Locate and identify every blood parasite.
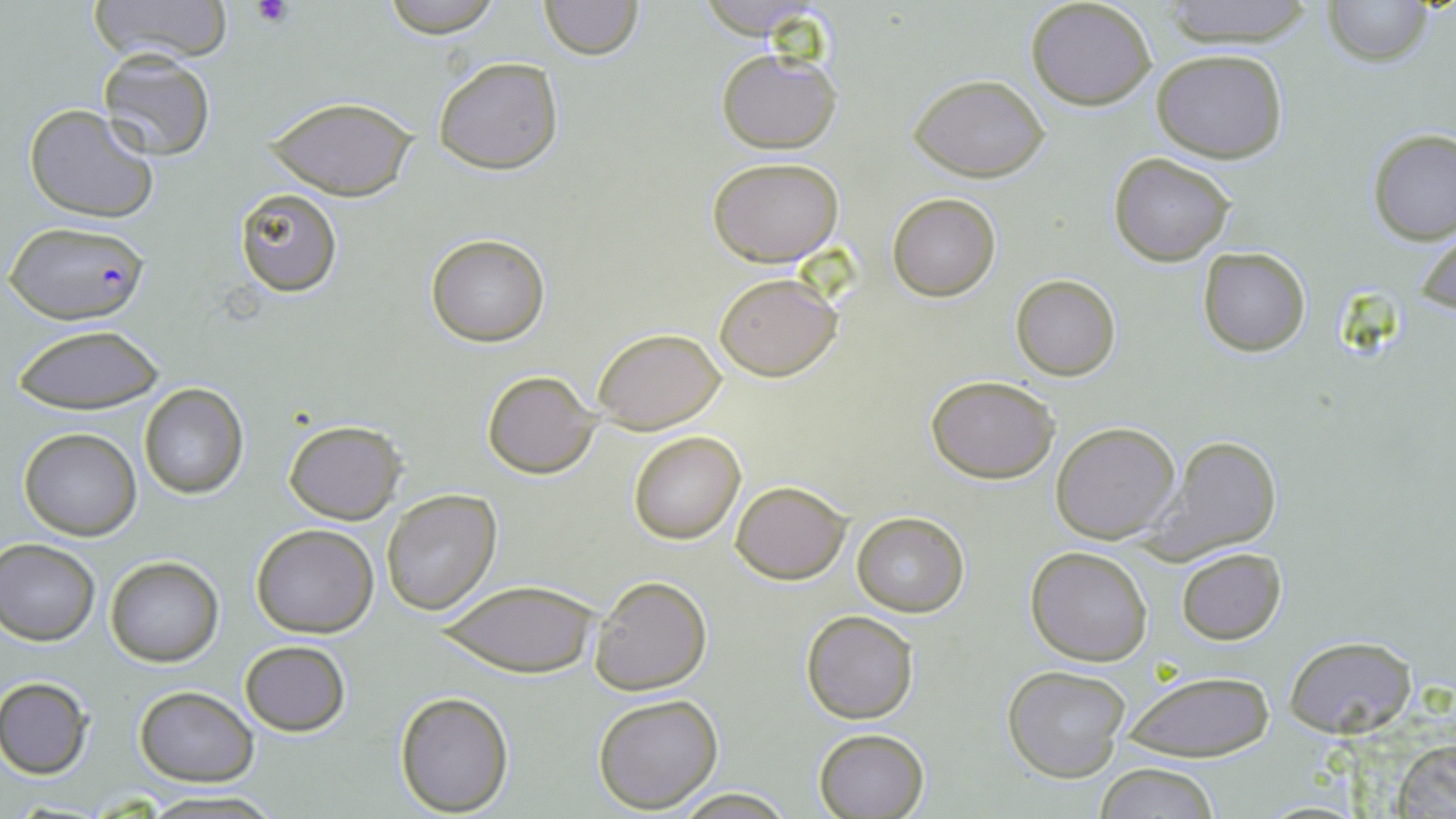

Approximate bounding boxes as (x1,y1)-(x2,y2) corner pairs in pixels.
Plasmodium falciparum-infected red blood cells: (3,220)-(150,325).
No Plasmodium ovale, Plasmodium malariae, Plasmodium vivax, Babesia divergens, or Trypanosoma brucei observed.

Uninfected red blood cell locations: (94,0)-(229,65), (376,0)-(508,39), (691,0)-(834,40), (1158,0)-(1318,47), (1323,0)-(1434,67), (537,1)-(644,60), (1025,1)-(1158,111), (716,48)-(842,154), (1153,49)-(1288,163), (96,50)-(216,161), (432,57)-(563,173), (909,73)-(1051,183), (267,96)-(416,201), (24,103)-(159,223), (1366,128)-(1455,243), (1108,153)-(1236,265), (707,157)-(845,266), (234,188)-(342,296), (887,193)-(1000,300), (1415,224)-(1456,322), (426,234)-(548,346), (1198,247)-(1310,355), (714,273)-(841,380), (1011,275)-(1121,381), (12,324)-(166,414), (593,326)-(727,434), (481,370)-(601,478), (924,373)-(1060,482), (138,385)-(248,498), (283,419)-(406,525), (1050,421)-(1181,544), (20,428)-(142,539), (628,429)-(747,545), (1149,436)-(1282,557), (730,480)-(849,584), (380,489)-(502,615), (852,511)-(969,617), (250,524)-(379,638), (0,539)-(100,644), (1024,546)-(1153,666), (1175,548)-(1286,644), (105,556)-(223,667), (587,573)-(712,697), (437,579)-(599,677), (801,610)-(919,722), (1284,635)-(1417,737), (239,640)-(351,737), (1003,665)-(1131,782), (1118,669)-(1276,763), (0,678)-(94,778), (132,688)-(259,785), (394,690)-(515,816), (591,691)-(723,813), (812,727)-(930,817), (1392,737)-(1456,818), (1093,764)-(1222,819), (669,788)-(796,818), (134,790)-(285,818). Platelet locations: (251,0)-(296,28). Slide-level diagnosis: Plasmodium falciparum. Thin blood smear. One field of a larger specimen. May-Grünwald-Giemsa stain. Image is 1456×819 pixels. Optical microscopy. 1000x magnification.